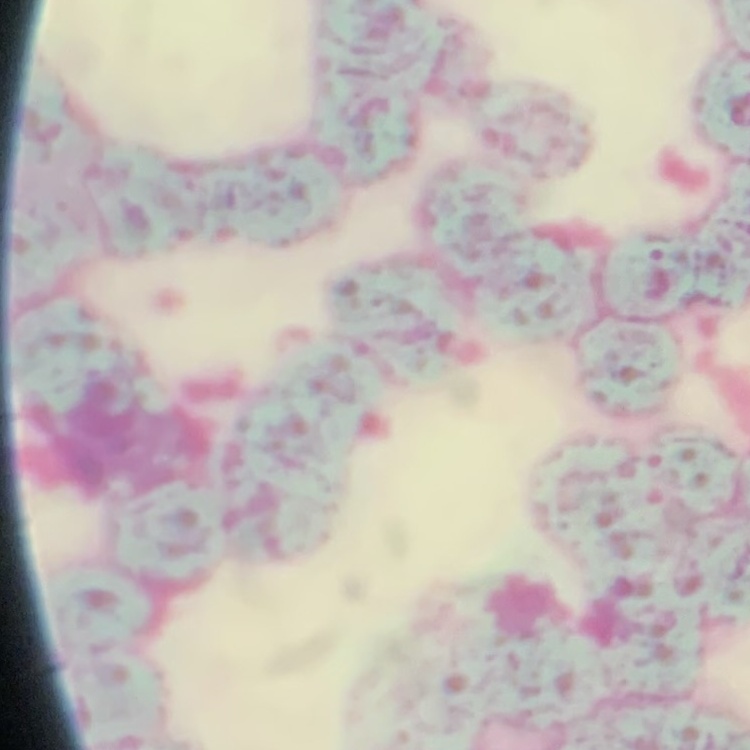
The red blood cells show rouleaux formation. Thin peripheral smear. Field's or Giemsa stain. Square crop of a larger photomicrograph.